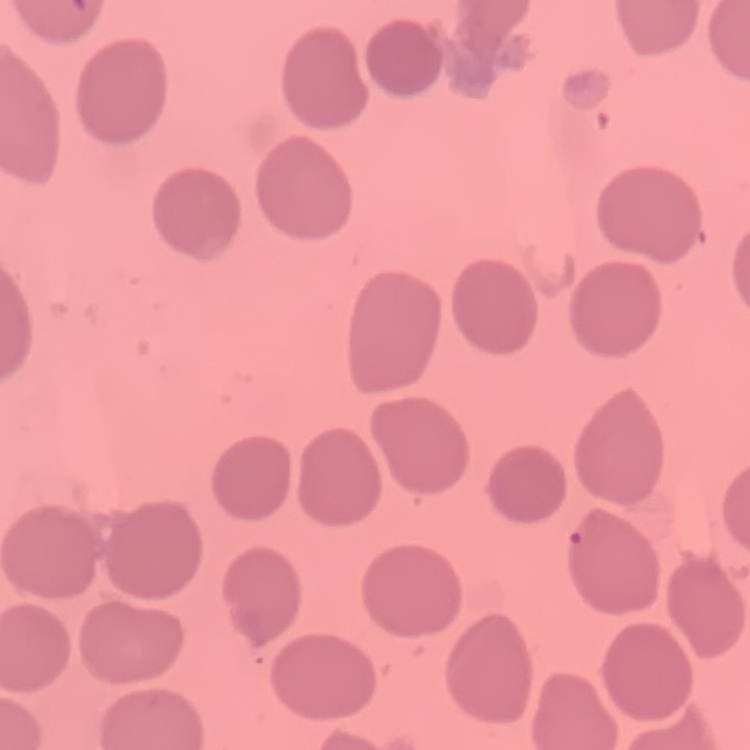

The erythrocytes show no rouleaux formation. Thin peripheral smear. Stained with either Field's or Giemsa. Square crop of a larger photomicrograph.